Identify the parasite.
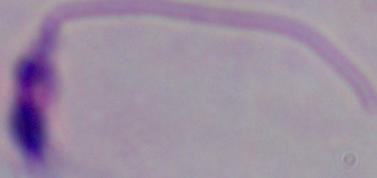
This is Leishmania.

magnification = 1000x
modality = photomicrograph